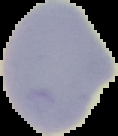

From a thin blood smear. Image is 118×136 pixels. Segmented cell region on a black background. Result: no Plasmodium parasites seen.